Identify the parasite.
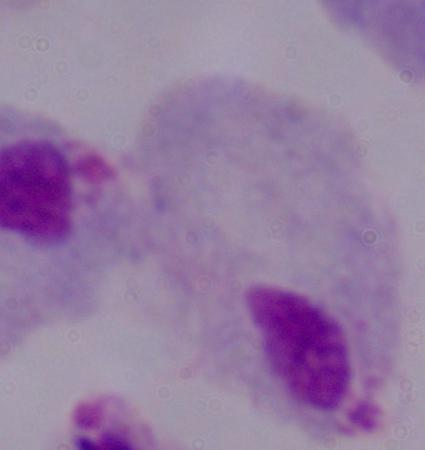

This is a trichomonad.

Summary:
  - Modality: micrograph
  - Magnification: 1000x